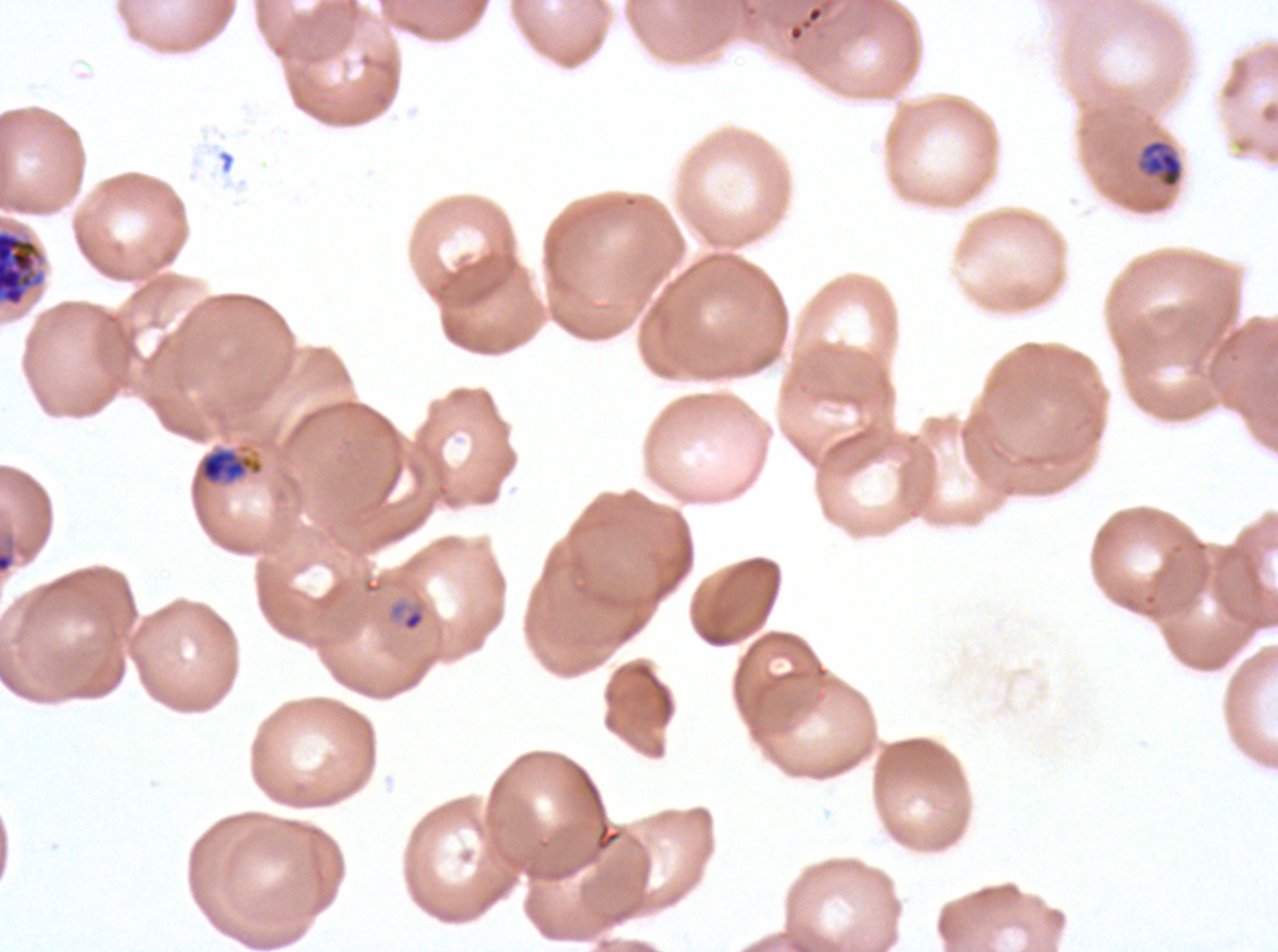

Approximate bounding rectangles given as corner coordinates in pixels from the top-left. Segmenter locations: (x1=0, y1=229, x2=44, y2=307). Late trophozoite locations: (x1=1135, y1=138, x2=1185, y2=190), (x1=197, y1=447, x2=264, y2=485). Late-ring/early-trophozoite locations: (x1=387, y1=600, x2=426, y2=633). Image is 1278×952 pixels. One sub-image of a larger composite. Life-cycle stages observed: late-ring/early-trophozoite, late trophozoite, segmenter. Giemsa stain. P. falciparum from a patient in The Gambia, cultured ex vivo for 24 to 48 hours. Thin blood film.